Classify this cell by malaria status.
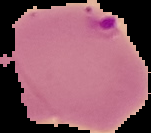

It is parasitized.

Image is 151×133 pixels. Segmented cell region on a black background. From a thin blood film.